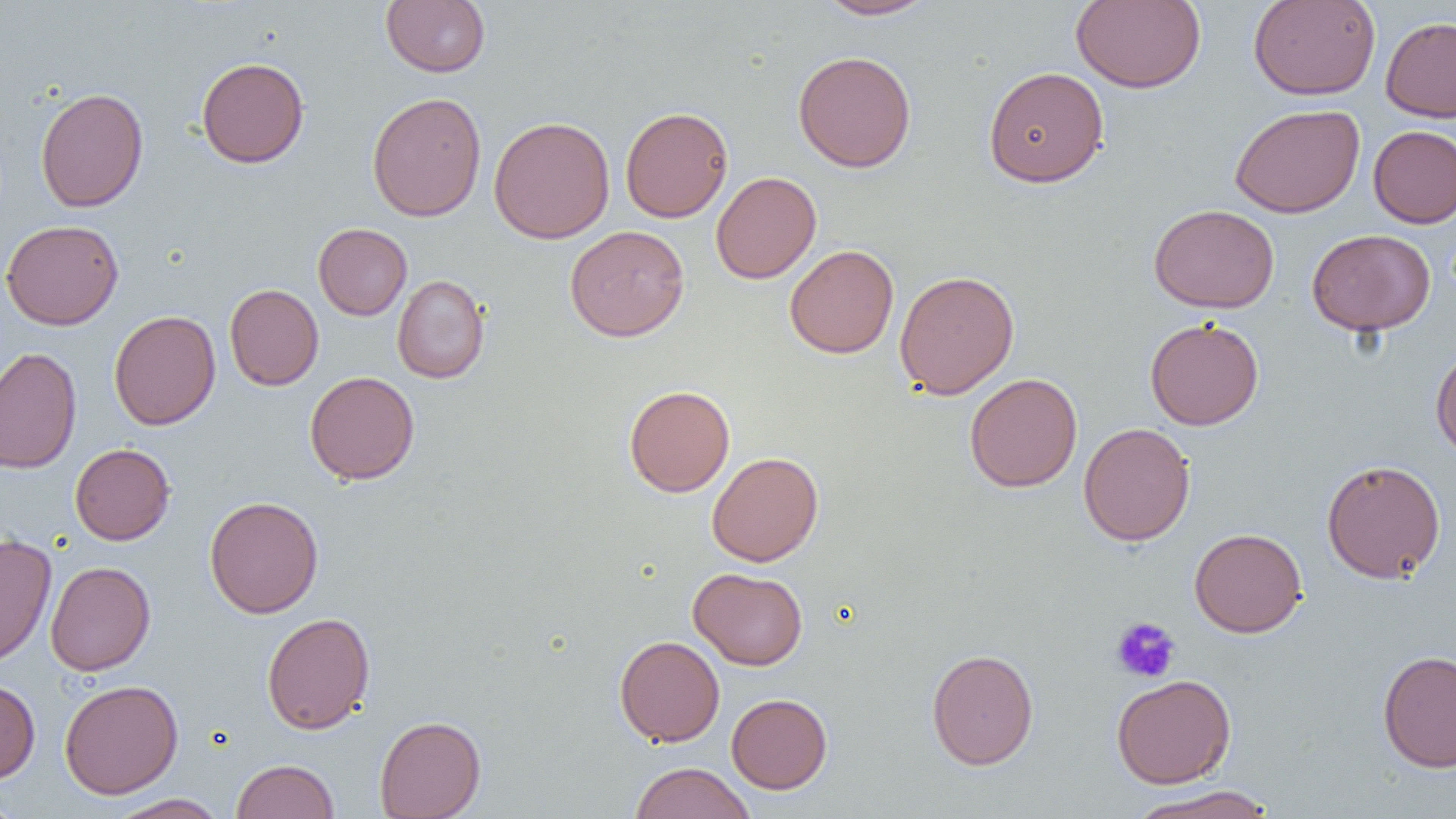

{
  "slide_level_diagnosis": "no evidence of blood parasites",
  "platelet_locations": "approximate bounding boxes as (x1, y1, x2, y2) in pixels: (1111, 617, 1181, 683)",
  "preparation": "thin blood smear",
  "image_size": "1456×819 pixels",
  "magnification": "1000x",
  "modality": "light microscopy",
  "field_of_view": "single",
  "uninfected_red_blood_cell_locations": "approximate bounding boxes as (x1, y1, x2, y2) in pixels: (816, 0, 938, 20), (1071, 0, 1206, 93), (1248, 0, 1381, 100), (381, 1, 491, 77), (1380, 16, 1456, 122), (793, 50, 916, 173), (196, 56, 309, 168), (983, 66, 1109, 187), (35, 87, 149, 213), (367, 91, 487, 222), (1229, 103, 1365, 218), (620, 105, 733, 222), (488, 115, 615, 244), (1368, 125, 1456, 227), (711, 171, 821, 284), (1149, 204, 1280, 313), (1, 219, 124, 330), (313, 223, 412, 320), (565, 225, 689, 341), (1307, 228, 1435, 335), (785, 244, 899, 359), (894, 269, 1020, 399), (392, 274, 490, 383), (224, 283, 324, 391), (108, 310, 221, 430), (1145, 317, 1264, 430), (1430, 345, 1456, 461), (0, 347, 82, 473), (305, 370, 419, 484), (964, 372, 1082, 493), (623, 385, 735, 497), (1078, 422, 1195, 546), (70, 443, 175, 545), (706, 451, 824, 566), (1321, 458, 1446, 583), (204, 496, 324, 618), (1189, 527, 1307, 638), (0, 533, 57, 668), (45, 561, 156, 676), (689, 567, 808, 670), (261, 612, 375, 735), (614, 635, 725, 746), (926, 648, 1039, 770), (1377, 649, 1456, 773), (1111, 674, 1236, 788), (0, 678, 40, 783), (59, 679, 184, 799), (726, 693, 832, 793), (374, 715, 486, 819), (230, 759, 339, 819), (629, 762, 756, 819), (1127, 785, 1277, 819), (0, 789, 23, 818), (108, 793, 229, 819)"
}